Locate and identify every blood parasite.
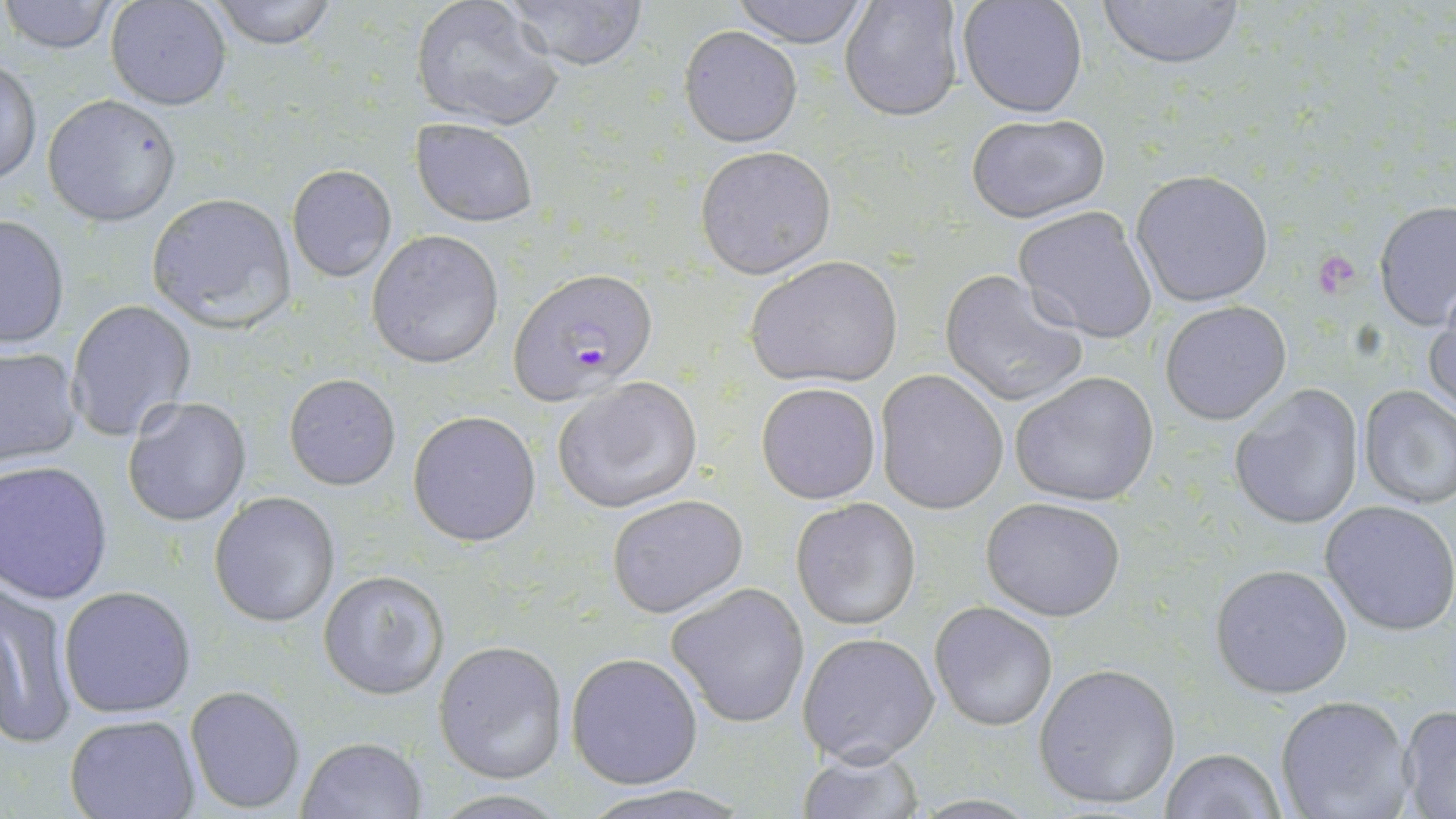

Approximate bounding boxes as (x1,y1)-(x2,y2) corner pairs in pixels.
Plasmodium falciparum-infected red blood cells: (512,269)-(653,407).
No Plasmodium ovale, Plasmodium malariae, Plasmodium vivax, Babesia divergens, or Trypanosoma brucei observed.

Summary:
  - Platelet locations: (1317,257)-(1359,297)
  - Uninfected red blood cell locations: (0,0)-(121,54), (104,0)-(233,111), (205,0)-(338,49), (498,0)-(649,70), (727,0)-(873,47), (955,0)-(1090,119), (1097,0)-(1247,71), (410,1)-(565,130), (840,2)-(965,122), (680,26)-(802,147), (1,58)-(41,185), (42,95)-(182,226), (965,112)-(1111,224), (410,118)-(539,228), (695,146)-(836,278), (286,165)-(396,282), (1131,169)-(1277,307), (144,191)-(299,332), (1372,201)-(1456,334), (1012,204)-(1159,344), (0,214)-(71,348), (366,229)-(504,367), (747,255)-(904,390), (939,269)-(1089,407), (1425,282)-(1456,420), (68,299)-(196,440), (1159,301)-(1294,425), (0,344)-(83,467), (874,369)-(1009,514), (1008,371)-(1160,507), (284,373)-(401,490), (551,376)-(703,515), (755,383)-(881,504), (1228,384)-(1366,533), (1356,385)-(1456,510), (123,397)-(252,526), (407,408)-(541,547), (1,460)-(114,603), (209,491)-(340,628), (607,493)-(749,618), (981,495)-(1129,622), (790,498)-(921,630), (1319,499)-(1456,636), (1209,563)-(1354,699), (319,570)-(449,700), (0,582)-(79,748), (665,582)-(810,728), (59,585)-(199,719), (929,601)-(1058,732), (797,631)-(939,766), (433,639)-(569,783), (566,652)-(701,788), (1033,662)-(1181,810), (184,685)-(306,814), (1273,694)-(1417,819), (1396,705)-(1456,818), (64,714)-(202,819), (297,735)-(428,818), (794,747)-(921,819), (1159,748)-(1286,819), (580,785)-(750,819)
  - Slide-level diagnosis: Plasmodium falciparum
  - Field of view: one of a larger specimen
  - Image size: 1456×819 pixels
  - Magnification: 1000x
  - Stain: May-Grünwald-Giemsa
  - Preparation: thin blood film
  - Modality: optical microscopy